Report the malaria status of this cell.
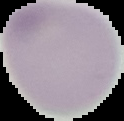
It is uninfected.

image size = 124×121 pixels
preparation = thin blood smear
image type = segmented cell region with the area outside set to black